Identify the blood parasite species.
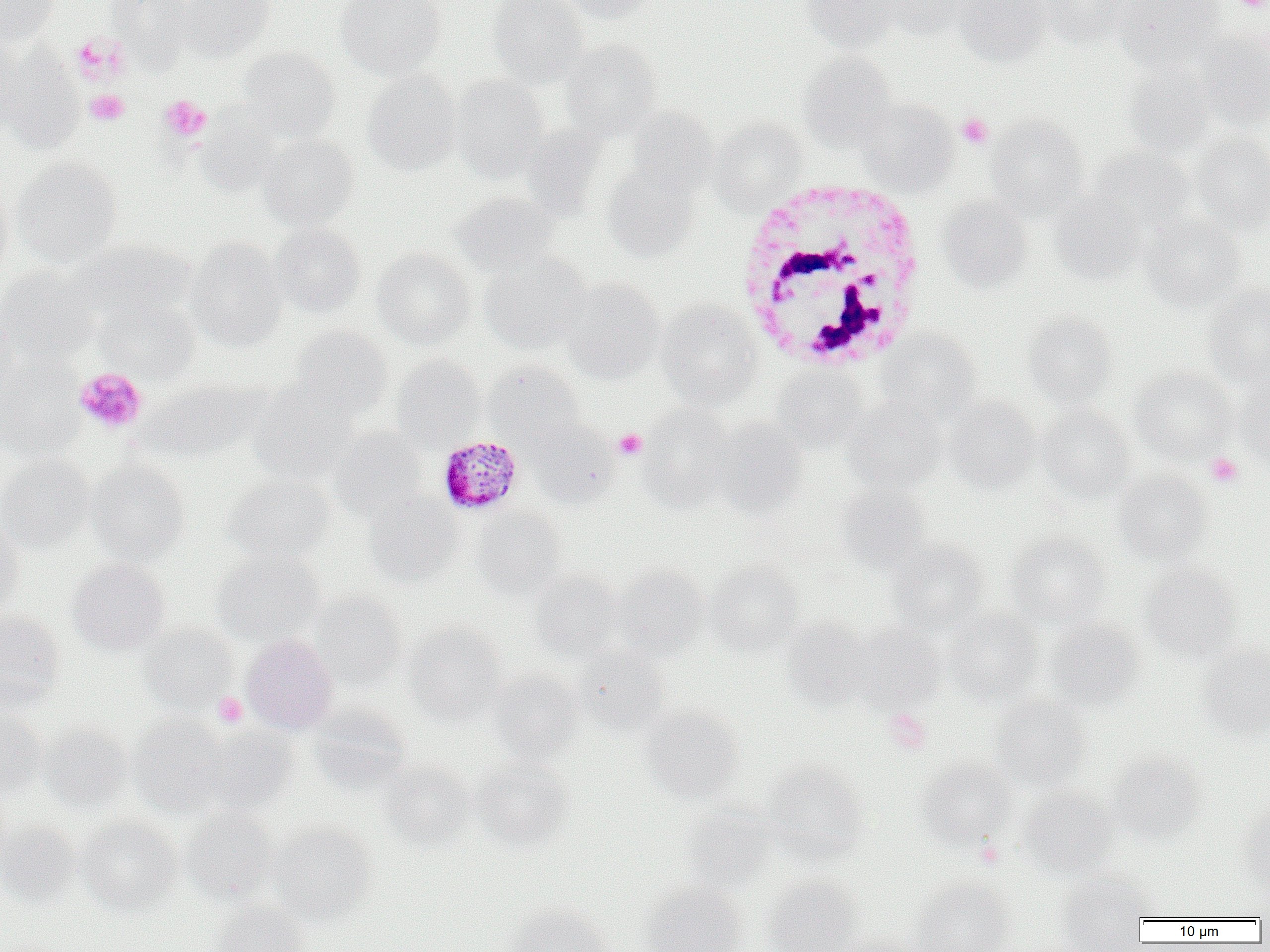
Plasmodium malariae.

Summary:
  - Coordinate format: approximate bounding boxes as [x1, y1, x2, y2] in pixels
  - Platelet locations: [1234, 0, 1268, 12], [70, 32, 131, 85], [85, 89, 129, 125], [159, 95, 211, 141], [957, 113, 994, 148], [74, 367, 147, 434], [614, 429, 646, 459], [1206, 453, 1242, 487], [213, 692, 247, 727], [883, 709, 930, 753], [975, 839, 1005, 868]
  - Uninfected red blood cell locations: [0, 0, 59, 44], [105, 0, 194, 67], [179, 0, 274, 61], [335, 0, 446, 79], [487, 0, 589, 88], [558, 0, 658, 23], [802, 0, 899, 51], [879, 0, 975, 39], [953, 0, 1051, 66], [1039, 0, 1135, 48], [1115, 0, 1223, 68], [1196, 29, 1270, 129], [561, 39, 662, 139], [0, 46, 85, 152], [238, 47, 339, 142], [798, 50, 897, 149], [1124, 63, 1215, 158], [362, 70, 461, 174], [451, 75, 549, 181], [857, 99, 958, 195], [627, 108, 716, 193], [195, 111, 280, 195], [987, 115, 1089, 218], [708, 118, 806, 212], [1189, 132, 1270, 235], [260, 134, 359, 230], [1086, 146, 1195, 236], [12, 157, 122, 268], [602, 163, 699, 261], [0, 187, 14, 283], [1050, 191, 1147, 284], [451, 192, 560, 277], [937, 197, 1031, 291], [1142, 214, 1246, 311], [270, 224, 365, 317], [185, 238, 287, 350], [78, 239, 193, 320], [372, 248, 476, 350], [480, 252, 591, 353], [0, 266, 99, 361], [561, 278, 665, 383], [1204, 284, 1270, 388], [94, 294, 200, 383], [656, 299, 763, 408], [1023, 312, 1117, 409], [0, 313, 18, 405], [289, 326, 392, 419], [877, 328, 982, 420], [391, 355, 486, 448], [0, 357, 84, 460], [483, 360, 585, 446], [773, 364, 868, 450], [1131, 367, 1235, 462], [140, 380, 257, 462], [247, 385, 359, 486], [1235, 390, 1270, 473], [944, 396, 1041, 492], [845, 398, 945, 492], [639, 404, 736, 509], [1037, 405, 1137, 501], [527, 419, 619, 507], [711, 419, 808, 516], [331, 426, 428, 520], [0, 455, 95, 551], [86, 458, 190, 564], [1111, 471, 1211, 563], [223, 474, 334, 564], [835, 484, 931, 572], [365, 493, 462, 585], [472, 506, 566, 599], [0, 519, 24, 616], [1005, 532, 1111, 628], [885, 541, 989, 635], [211, 550, 323, 644], [68, 559, 170, 654], [706, 560, 803, 656], [614, 564, 709, 658], [1140, 564, 1242, 662], [529, 569, 624, 663], [310, 591, 407, 687], [944, 609, 1044, 704], [0, 610, 65, 709], [781, 617, 871, 709], [1046, 619, 1145, 710], [405, 622, 507, 725], [846, 623, 945, 712], [138, 624, 237, 711], [241, 634, 338, 734], [1197, 642, 1270, 740], [574, 646, 669, 736], [487, 669, 585, 763], [990, 695, 1091, 793], [309, 704, 411, 792], [639, 706, 744, 804], [0, 709, 47, 798], [129, 713, 229, 816], [40, 721, 134, 813], [198, 726, 298, 813], [1106, 751, 1205, 843], [471, 758, 573, 851], [917, 758, 1018, 849], [379, 761, 475, 850], [762, 761, 870, 861], [1018, 786, 1121, 877], [682, 803, 777, 894], [1237, 805, 1270, 893], [180, 806, 277, 903], [78, 817, 181, 915], [0, 820, 81, 907], [269, 822, 376, 923], [1057, 872, 1153, 951], [762, 873, 866, 952], [912, 878, 1015, 952], [641, 881, 748, 952], [210, 900, 310, 952], [503, 903, 612, 952], [830, 934, 924, 952]
  - White blood cell locations: [734, 178, 932, 374]
  - Plasmodium malariae-infected red blood cell locations: [435, 436, 522, 517]
  - Image size: 1270×952 pixels
  - Magnification: 1000x
  - Field of view: one of a larger specimen
  - Preparation: thin blood film
  - Modality: light microscopy